Identify the parasite.
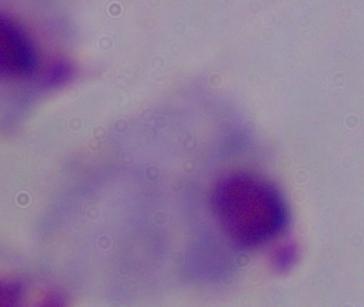
This is a trichomonad.

Summary:
  - Magnification: 1000x
  - Modality: photomicrograph